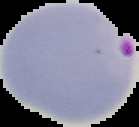
Summary:
  - Image size: 139×127 pixels
  - Malaria status: parasitized
  - Image type: segmented cell region with the area outside set to black
  - Preparation: thin blood film